Report the malaria status of this cell.
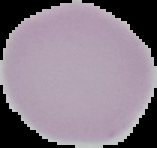

It is uninfected.

{
  "image_type": "cell region segmented out of the field of view; surrounding area masked to black",
  "preparation": "thin blood film",
  "image_size": "157×148 pixels"
}